Locate every leukocyte (white blood cell).
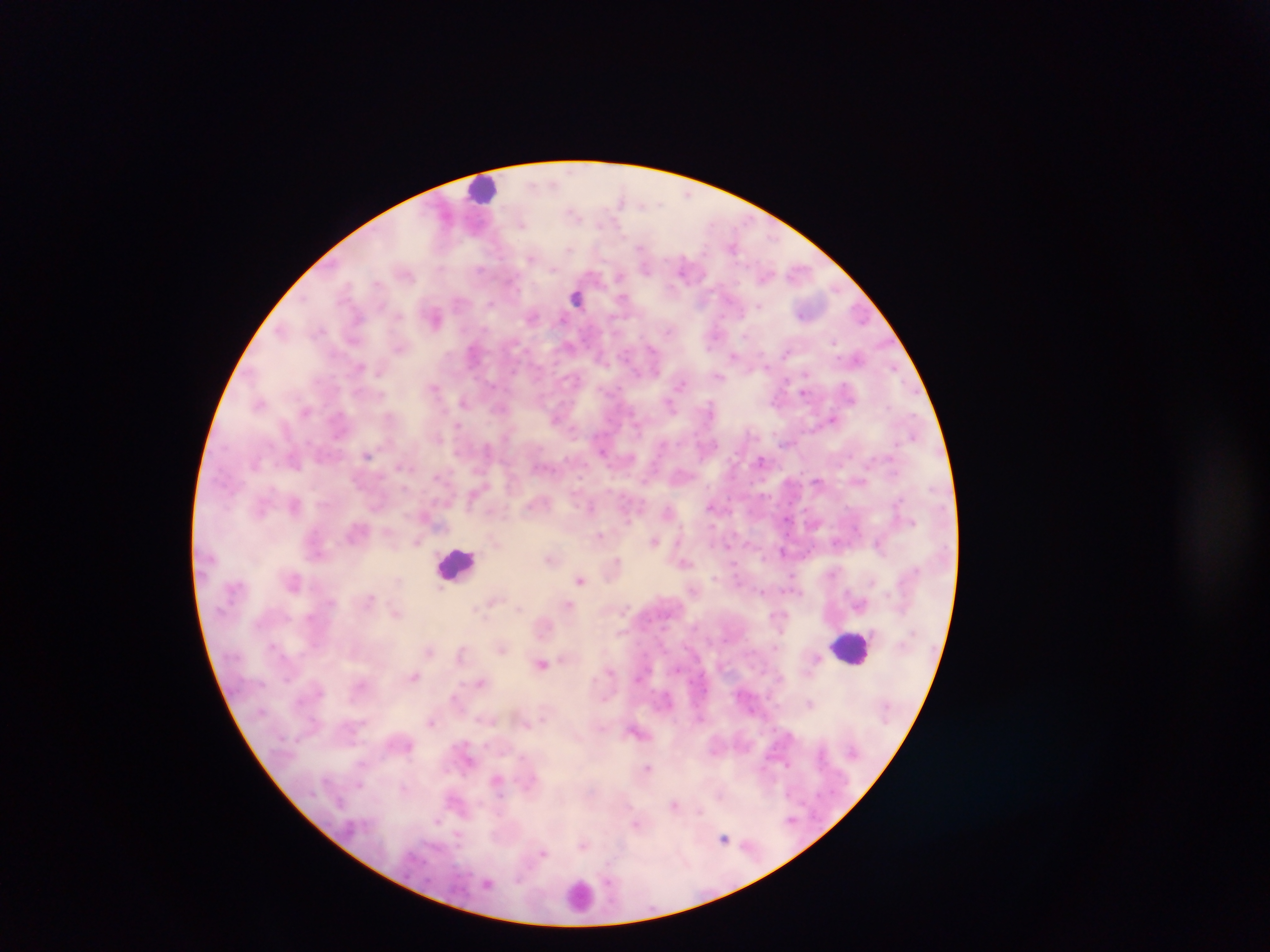

Approximate centers as [x, y] in pixels.
Leukocytes: [483, 189], [576, 297], [457, 563], [853, 648], [579, 895].

Summary:
  - Malaria parasite locations: [688, 196], [620, 200], [659, 203], [643, 204], [573, 213], [522, 225], [732, 247], [570, 248], [641, 248], [531, 258], [683, 267], [646, 268], [553, 269], [480, 270], [406, 275], [620, 276], [377, 283], [512, 285], [347, 287], [621, 298], [490, 304], [759, 306], [397, 315], [436, 317], [358, 318], [532, 318], [320, 329], [282, 331], [668, 331], [745, 336], [834, 341], [399, 348], [652, 350], [786, 352], [472, 353], [733, 356], [857, 357], [359, 368], [895, 370], [718, 377], [576, 380], [681, 385], [434, 388], [803, 393], [381, 395], [463, 401], [259, 404], [669, 406], [709, 406], [888, 407], [305, 410], [389, 416], [833, 418], [458, 425], [573, 428], [913, 436], [602, 451], [367, 454], [761, 460], [400, 467], [437, 477], [817, 480], [294, 505], [711, 507], [590, 508], [260, 510], [667, 510], [787, 520], [601, 535], [654, 541], [416, 542], [877, 544], [729, 545], [782, 551], [549, 559], [618, 560], [684, 563], [714, 577], [580, 580], [872, 581], [440, 588], [762, 592], [371, 597], [492, 600], [569, 605], [517, 608], [476, 609], [396, 613], [778, 615], [501, 649], [429, 651], [460, 653], [817, 658], [542, 663], [609, 671], [413, 677], [480, 682], [454, 698], [809, 703], [431, 722], [786, 764], [648, 767], [497, 780], [358, 784], [404, 787], [720, 796], [340, 802], [674, 805], [699, 811], [791, 820], [437, 821], [636, 823], [458, 837], [724, 838], [583, 845], [543, 853], [608, 882], [487, 884]
  - Country: Ghana
  - Image size: 1270×952 pixels
  - Capture: mobile-phone photograph through a microscope
  - Field of view: single
  - Preparation: thick blood film